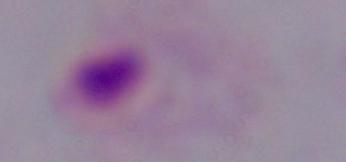

magnification = 1000x
modality = micrograph
identification = trichomonad